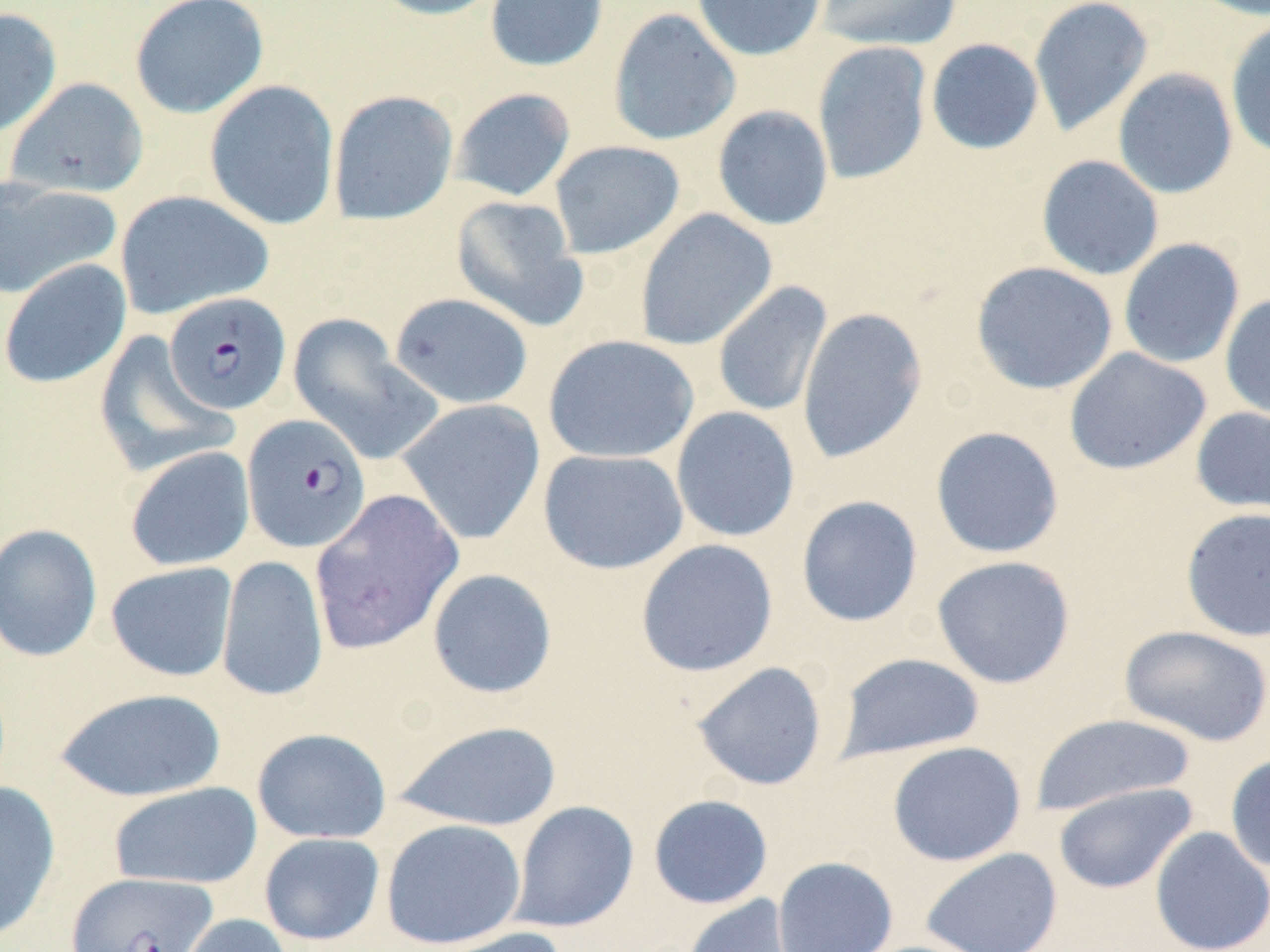

Summary:
  - Coordinate format: approximate bounding boxes as [x1, y1, x2, y2] in pixels
  - Plasmodium falciparum-infected red blood cell locations: [163, 292, 291, 415], [241, 414, 371, 553], [65, 871, 217, 952]
  - Uninfected red blood cell locations: [129, 0, 269, 119], [369, 0, 507, 20], [484, 0, 609, 72], [691, 0, 827, 62], [816, 0, 962, 51], [1028, 0, 1154, 137], [1185, 0, 1270, 21], [0, 7, 62, 139], [608, 8, 741, 146], [1225, 20, 1270, 160], [926, 38, 1044, 155], [812, 41, 932, 185], [1113, 68, 1238, 199], [5, 77, 148, 199], [204, 80, 340, 231], [450, 87, 576, 202], [328, 89, 459, 226], [712, 105, 834, 231], [549, 140, 685, 260], [1036, 155, 1164, 281], [0, 176, 121, 300], [114, 189, 274, 320], [451, 194, 587, 331], [635, 208, 777, 351], [1118, 238, 1245, 369], [0, 258, 132, 389], [971, 261, 1118, 394], [712, 281, 833, 419], [389, 293, 533, 409], [1220, 294, 1270, 420], [797, 307, 927, 464], [288, 314, 442, 466], [93, 332, 238, 478], [543, 334, 699, 464], [1064, 348, 1211, 475], [396, 398, 546, 545], [1190, 405, 1270, 520], [671, 406, 800, 543], [930, 425, 1065, 559], [125, 445, 255, 572], [538, 448, 689, 574], [309, 489, 464, 655], [796, 495, 923, 627], [1180, 507, 1270, 642], [0, 522, 103, 663], [635, 538, 778, 677], [216, 555, 328, 703], [931, 555, 1077, 689], [104, 561, 238, 682], [426, 568, 558, 699], [1118, 625, 1270, 747], [834, 652, 986, 762], [691, 661, 828, 791], [54, 687, 227, 802], [1029, 714, 1198, 817], [393, 719, 563, 831], [252, 727, 391, 844], [887, 741, 1026, 867], [1225, 753, 1270, 873], [0, 781, 61, 943], [108, 782, 263, 889], [1052, 782, 1198, 894], [648, 794, 774, 909], [508, 800, 639, 933], [380, 818, 527, 950], [1150, 827, 1270, 952], [259, 833, 385, 945], [920, 847, 1063, 952], [772, 856, 898, 952], [681, 894, 805, 952], [173, 913, 294, 952], [420, 926, 570, 952]
  - Slide-level diagnosis: Plasmodium falciparum
  - Stain: May-Grünwald-Giemsa
  - Magnification: 1000x
  - Preparation: thin blood smear
  - Modality: optical microscopy
  - Image size: 1270×952 pixels
  - Field of view: single